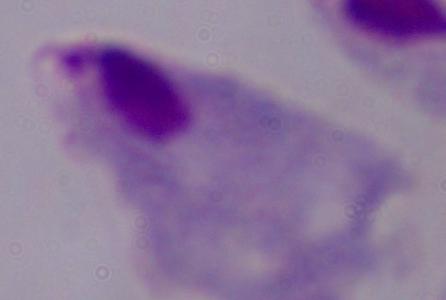
Summary:
  - Identification: trichomonad
  - Modality: micrograph
  - Magnification: 1000x